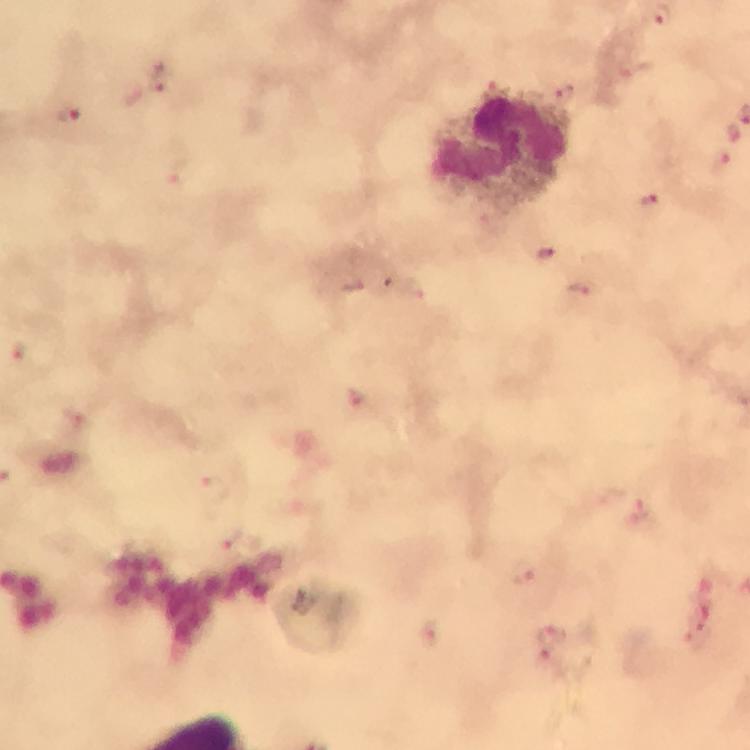

immersion_oil: used
stain: Giemsa
magnification: 100x
cropped_from: a single field of view
preparation: thick smear
plasmodium_parasite_locations: 'approximate object centers, in pixels from the top-left corner: (x=163, y=83), (x=495, y=88), (x=565, y=92), (x=71, y=117), (x=736, y=132), (x=719, y=164), (x=178, y=175), (x=651, y=204), (x=544, y=254), (x=414, y=290), (x=582, y=290), (x=360, y=405), (x=640, y=511), (x=524, y=573), (x=428, y=635), (x=550, y=638)'
leukocyte_locations: 'approximate object centers, in pixels from the top-left corner: (x=501, y=149)'
image_size: 750×750 pixels
capture: smartphone camera through the microscope
context: from a diagnostic examination for malaria